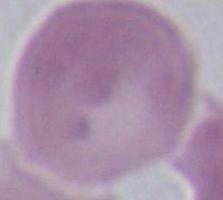
An erythrocyte is seen. Micrograph. Captured at 1000x magnification.